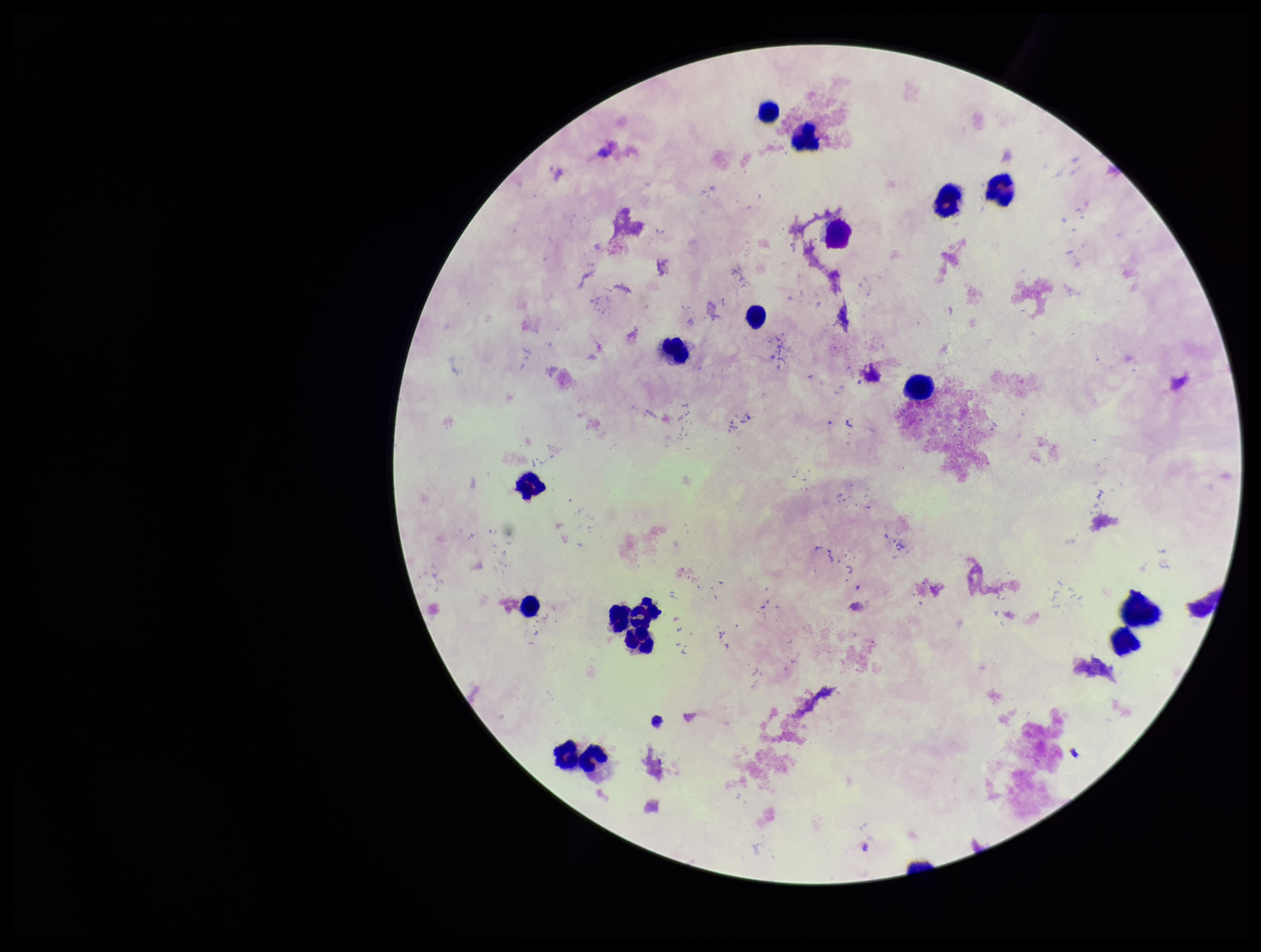
Preparation: thick. Photographed through the microscope eyepiece with a smartphone camera. Parasite count: 0. Plasmodium parasites: none identified. Giemsa stain. Patient malaria status: negative. One field from this slide. Image is 1261×952 pixels. Leukocyte count: 17.